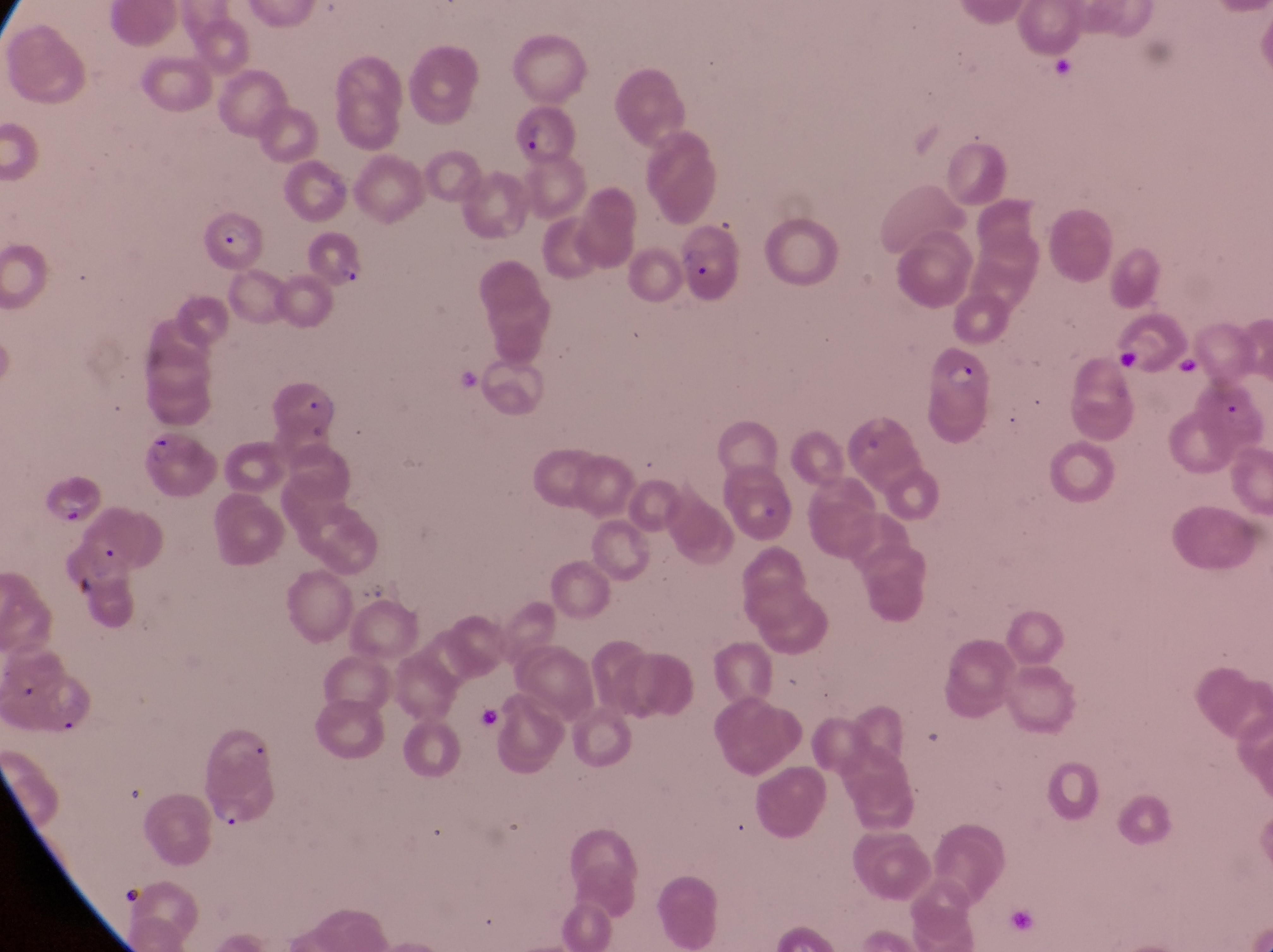

Approximate bounding boxes as {left, top, right, bottom} in pixels. Parasitised red blood cell locations: {510, 104, 577, 162}, {202, 210, 269, 275}, {302, 220, 376, 287}, {671, 220, 745, 303}, {929, 339, 998, 437}, {262, 374, 352, 446}, {142, 417, 217, 502}, {50, 482, 105, 529}. At a magnification of 1000x. Single field of view. Image is 1273×952 pixels. Sample from Uganda. Photographed through the eyepiece of an Olympus CX-23 microscope with a smartphone camera. Thin blood film.